Point out each malaria parasite.
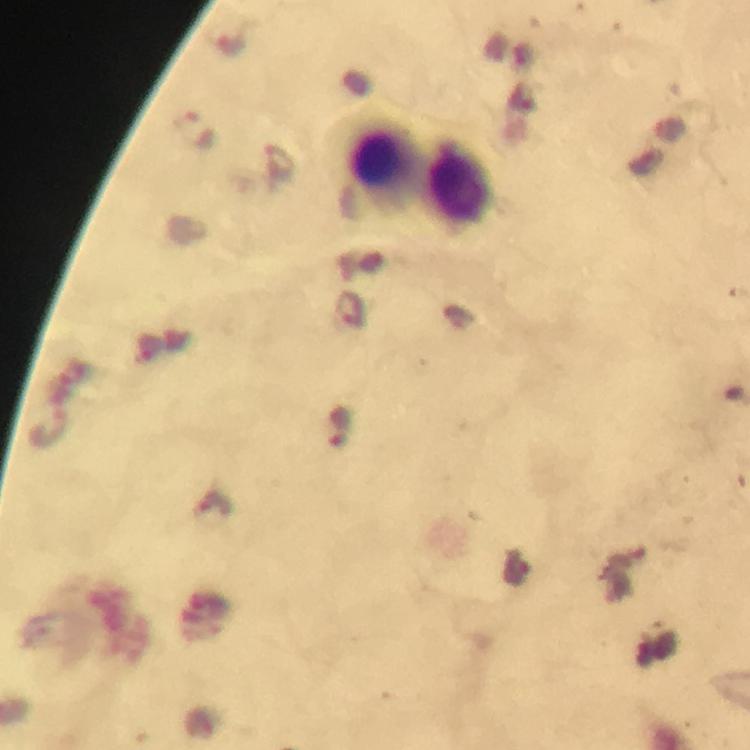
Approximate centers as {x, y} in pixels.
Malaria parasites: {195, 129}, {351, 309}, {340, 426}.

immersion_oil: used
magnification: 100x
cropped_from: a single field of view
image_size: 750×750 pixels
context: from a malaria diagnostic workup
preparation: thick blood smear
stain: Giemsa
leukocyte_locations: 'approximate centers as {x, y} in pixels: {379, 160}, {459, 184}'
capture: smartphone photograph through a microscope